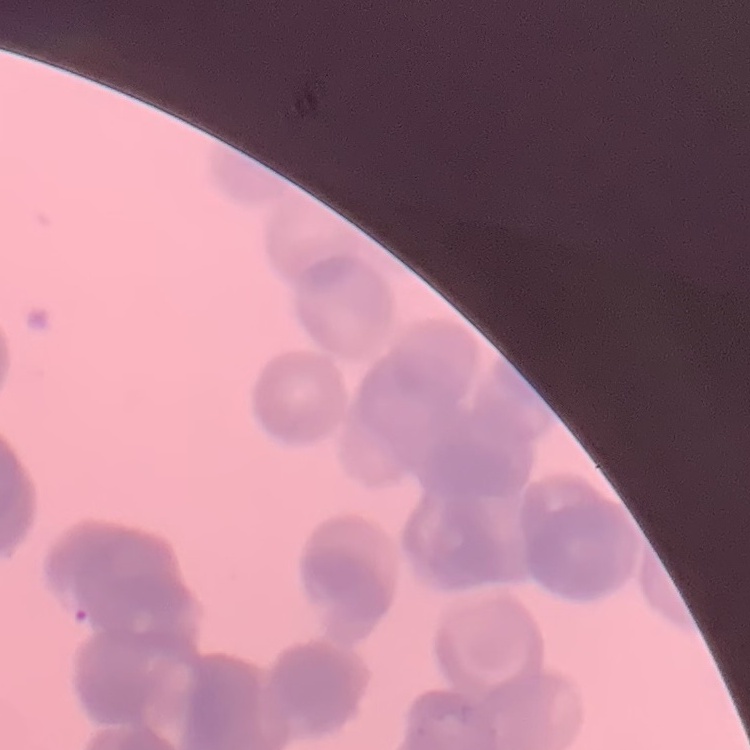
{
  "erythrocyte_morphology": "rouleaux formation",
  "stain": "Field's or Giemsa",
  "preparation": "thin peripheral smear",
  "image_type": "square crop of a larger photomicrograph"
}